Evaluate for malaria.
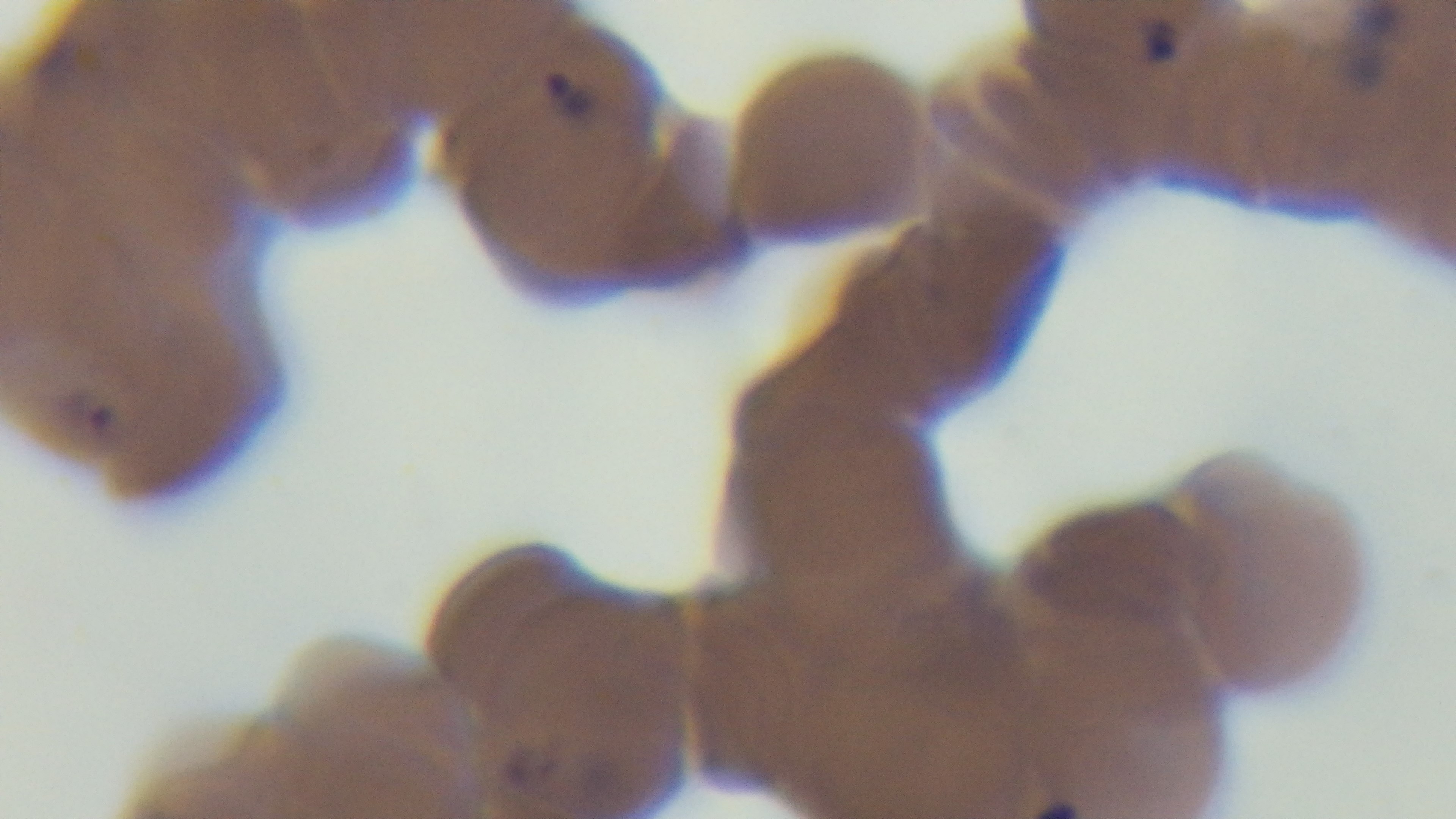
Infected.

preparation = thin smear
stain = Giemsa
modality = light microscopy
capture = mounted 4K digital camera
field of view = single
objective = 100x oil immersion